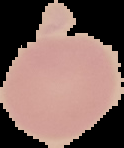 From a thin blood film. Result: negative for malaria parasites. Cell region segmented out of the field of view; the surrounding area is masked to black. Image is 124×148 pixels.